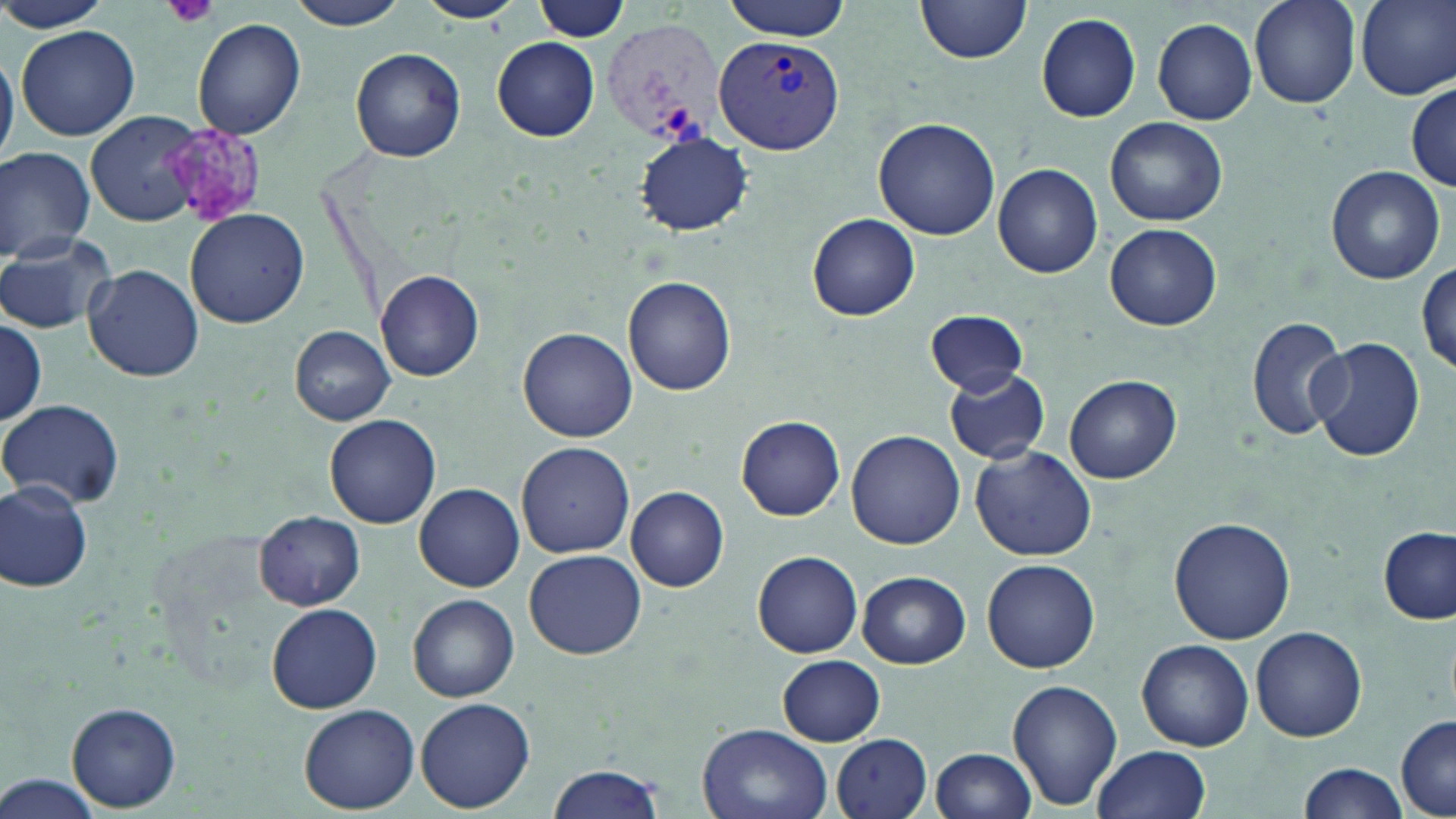

Approximate bounding boxes as [x1, y1, x2, y2] in pixels. Platelet locations: [164, 0, 222, 30], [167, 127, 264, 228]. Uninfected red blood cell locations: [0, 0, 116, 32], [286, 0, 410, 30], [415, 0, 523, 23], [533, 0, 629, 42], [722, 0, 850, 41], [1249, 0, 1360, 110], [1356, 0, 1456, 100], [916, 1, 1032, 67], [1036, 13, 1140, 123], [1153, 17, 1259, 125], [193, 19, 305, 141], [16, 25, 141, 141], [493, 38, 601, 142], [0, 48, 18, 167], [350, 48, 466, 162], [1408, 82, 1456, 191], [87, 110, 208, 227], [1105, 116, 1228, 226], [874, 117, 1001, 241], [635, 134, 751, 235], [0, 145, 96, 263], [993, 163, 1102, 278], [1325, 166, 1446, 285], [184, 208, 309, 328], [807, 214, 920, 320], [1105, 223, 1221, 331], [0, 233, 118, 334], [1416, 258, 1454, 375], [84, 264, 204, 384], [376, 270, 484, 382], [624, 275, 736, 397], [926, 310, 1029, 395], [1245, 315, 1351, 440], [0, 321, 48, 423], [289, 326, 396, 424], [520, 328, 637, 441], [1310, 335, 1426, 464], [942, 367, 1050, 465], [1065, 374, 1181, 484], [1, 397, 127, 510], [324, 414, 442, 528], [736, 416, 845, 521], [846, 429, 965, 548], [516, 441, 635, 558], [970, 446, 1096, 561], [0, 477, 95, 595], [415, 483, 524, 591], [627, 486, 729, 592], [255, 511, 365, 609], [1168, 517, 1295, 645], [1379, 528, 1455, 624], [524, 548, 646, 660], [753, 551, 864, 657], [983, 559, 1101, 674], [857, 570, 970, 669], [409, 593, 519, 702], [266, 603, 382, 714], [1251, 626, 1367, 742], [1136, 639, 1253, 751], [777, 654, 885, 746], [1007, 680, 1122, 809], [416, 697, 535, 812], [67, 702, 182, 812], [299, 704, 420, 814], [1396, 713, 1455, 818], [697, 724, 833, 819], [832, 733, 934, 819], [1091, 745, 1211, 819], [930, 748, 1038, 819], [1297, 761, 1408, 818], [546, 764, 664, 819], [1, 772, 105, 818]. Plasmodium vivax-infected red blood cell locations: [601, 15, 724, 147], [713, 32, 840, 155]. Slide-level diagnosis: Plasmodium vivax. 1000x magnification. Light microscopy. Image is 1456×819 pixels. May-Grünwald-Giemsa stain. Thin blood film. One field of a larger specimen.